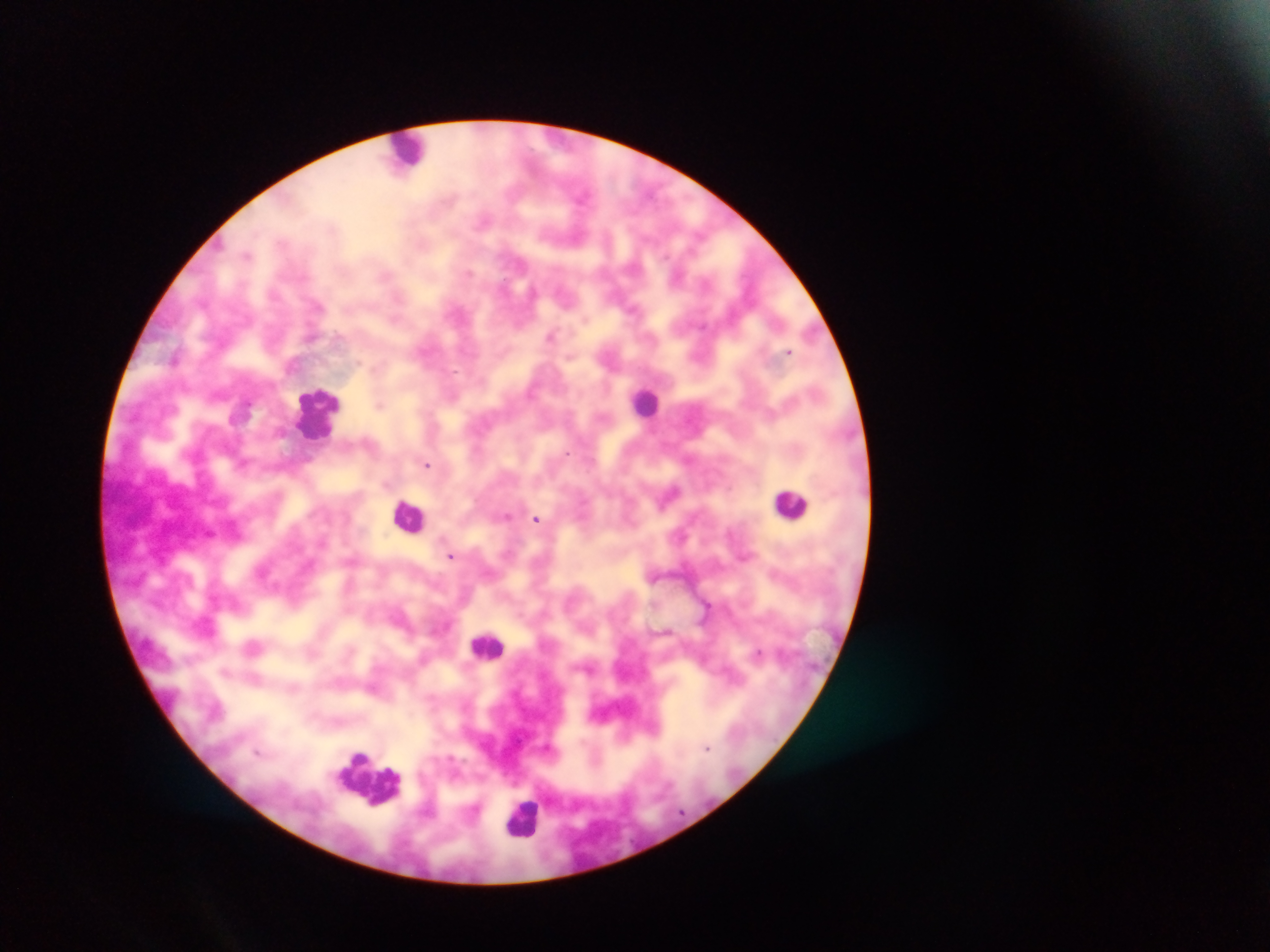

field of view = single
capture = mobile-phone photograph through a microscope
leukocyte locations = approximate centers as {x, y} in pixels: {408, 151}, {645, 401}, {315, 412}, {791, 504}, {410, 515}, {488, 646}, {371, 778}, {523, 816}
image size = 1270×952 pixels
country = Ghana
preparation = thick blood film
malaria parasite locations = approximate centers as {x, y} in pixels: {583, 194}, {483, 221}, {247, 255}, {468, 272}, {385, 274}, {676, 276}, {532, 292}, {318, 305}, {633, 309}, {394, 320}, {550, 335}, {789, 352}, {359, 362}, {380, 405}, {567, 453}, {427, 464}, {670, 493}, {506, 516}, {536, 519}, {681, 535}, {451, 556}, {759, 653}, {224, 671}, {707, 747}, {258, 751}